Give the extent of all uninfected red blood cells.
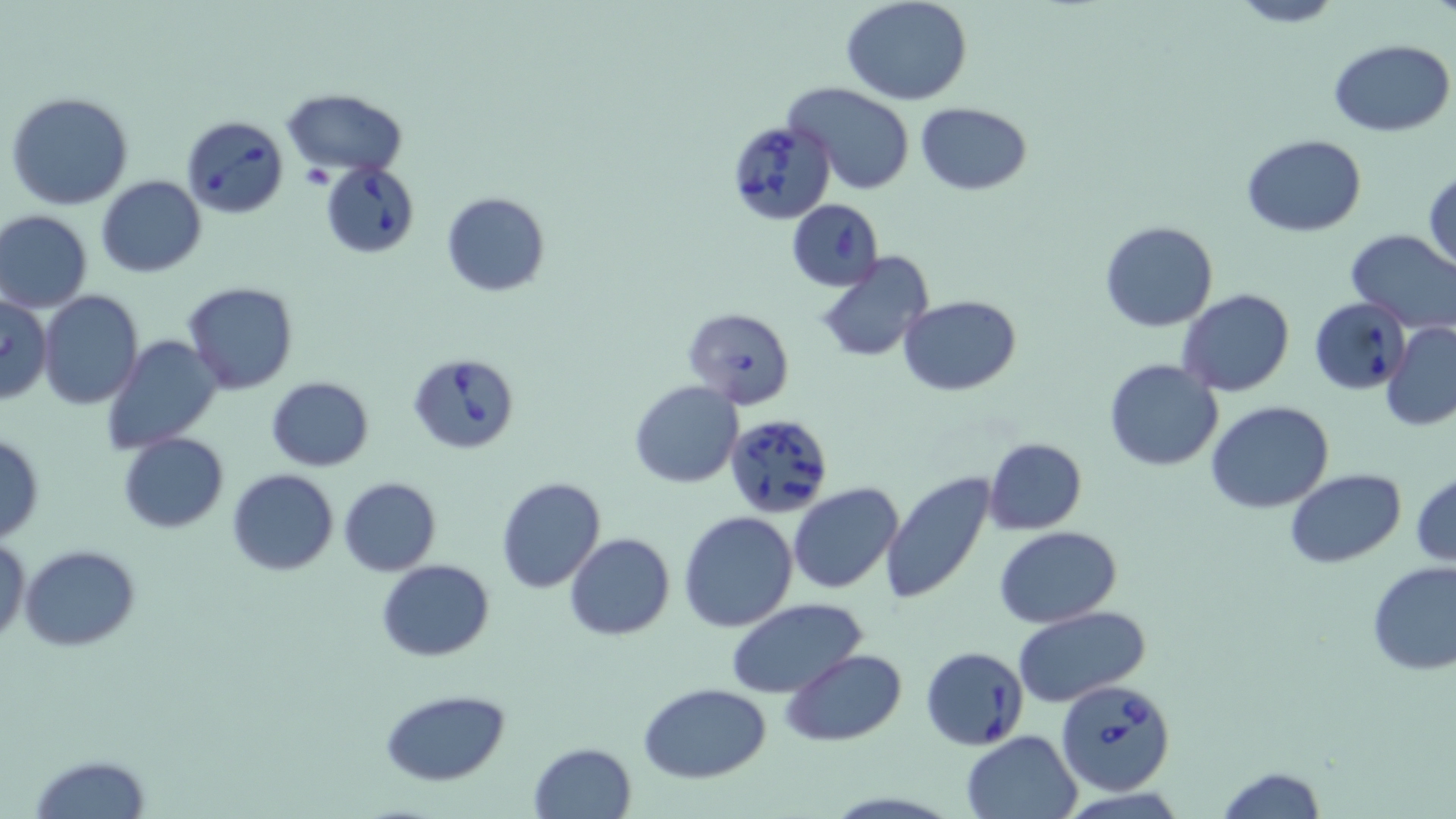
Approximate bounding boxes as named x1/y1/x2/y2 corners in pixels.
Uninfected red blood cells: (x1=841, y1=0, x2=972, y2=105), (x1=1225, y1=0, x2=1345, y2=28), (x1=1329, y1=39, x2=1455, y2=136), (x1=785, y1=83, x2=917, y2=199), (x1=283, y1=88, x2=407, y2=177), (x1=5, y1=93, x2=133, y2=211), (x1=917, y1=102, x2=1032, y2=195), (x1=1243, y1=135, x2=1366, y2=236), (x1=1425, y1=169, x2=1456, y2=274), (x1=96, y1=176, x2=206, y2=278), (x1=440, y1=191, x2=551, y2=297), (x1=0, y1=210, x2=92, y2=313), (x1=1100, y1=220, x2=1218, y2=332), (x1=1347, y1=229, x2=1456, y2=333), (x1=817, y1=252, x2=934, y2=363), (x1=181, y1=282, x2=299, y2=394), (x1=1177, y1=289, x2=1294, y2=396), (x1=38, y1=292, x2=145, y2=410), (x1=898, y1=292, x2=1021, y2=396), (x1=0, y1=295, x2=52, y2=406), (x1=1381, y1=322, x2=1456, y2=431), (x1=103, y1=335, x2=223, y2=454), (x1=1103, y1=359, x2=1223, y2=470), (x1=266, y1=378, x2=375, y2=472), (x1=630, y1=380, x2=744, y2=488), (x1=1206, y1=402, x2=1333, y2=514), (x1=0, y1=431, x2=46, y2=544), (x1=119, y1=432, x2=229, y2=532), (x1=984, y1=438, x2=1088, y2=534), (x1=1284, y1=467, x2=1408, y2=567), (x1=228, y1=469, x2=339, y2=576), (x1=880, y1=472, x2=997, y2=608), (x1=1410, y1=474, x2=1456, y2=566), (x1=495, y1=476, x2=606, y2=593), (x1=337, y1=477, x2=442, y2=575), (x1=788, y1=483, x2=904, y2=596), (x1=679, y1=510, x2=798, y2=631), (x1=994, y1=526, x2=1123, y2=628), (x1=565, y1=533, x2=674, y2=641), (x1=0, y1=537, x2=29, y2=647), (x1=20, y1=544, x2=141, y2=653), (x1=376, y1=559, x2=494, y2=662), (x1=1366, y1=561, x2=1455, y2=674), (x1=725, y1=598, x2=868, y2=699), (x1=1012, y1=605, x2=1152, y2=707), (x1=783, y1=650, x2=909, y2=744), (x1=638, y1=684, x2=771, y2=782), (x1=378, y1=689, x2=513, y2=785), (x1=961, y1=728, x2=1083, y2=819), (x1=528, y1=742, x2=637, y2=819), (x1=30, y1=753, x2=152, y2=819), (x1=1217, y1=765, x2=1326, y2=819).

slide-level diagnosis = Babesia divergens
platelet locations = approximate bounding boxes as named x1/y1/x2/y2 corners in pixels: (x1=296, y1=164, x2=332, y2=190)
Babesia divergens-infected red blood cell locations = approximate bounding boxes as named x1/y1/x2/y2 corners in pixels: (x1=181, y1=114, x2=290, y2=217), (x1=726, y1=120, x2=839, y2=224), (x1=320, y1=163, x2=420, y2=258), (x1=788, y1=196, x2=884, y2=292), (x1=1307, y1=300, x2=1412, y2=405), (x1=685, y1=307, x2=798, y2=409), (x1=408, y1=353, x2=521, y2=455), (x1=725, y1=412, x2=835, y2=518), (x1=920, y1=647, x2=1030, y2=750), (x1=1057, y1=678, x2=1175, y2=796)
image size = 1456×819 pixels
field of view = one of a larger specimen
stain = May-Grünwald-Giemsa
preparation = thin blood film
magnification = 1000x
modality = optical microscopy